State which parasite is depicted.
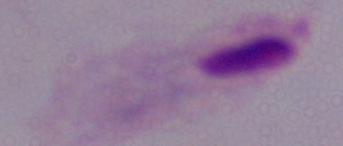
This is a trichomonad.

Summary:
  - Magnification: 1000x
  - Modality: photomicrograph